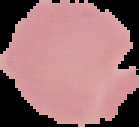

preparation = thin blood film
image type = cell region segmented out of the field of view; surrounding area masked to black
malaria status = uninfected
image size = 139×127 pixels